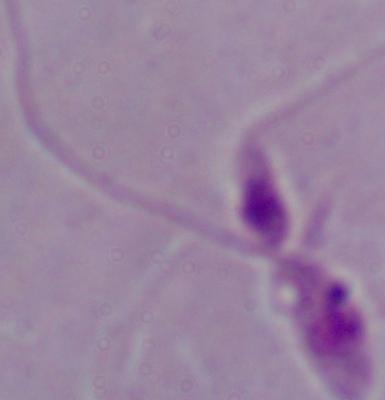
magnification: 1000x
identification: Leishmania
modality: photomicrograph